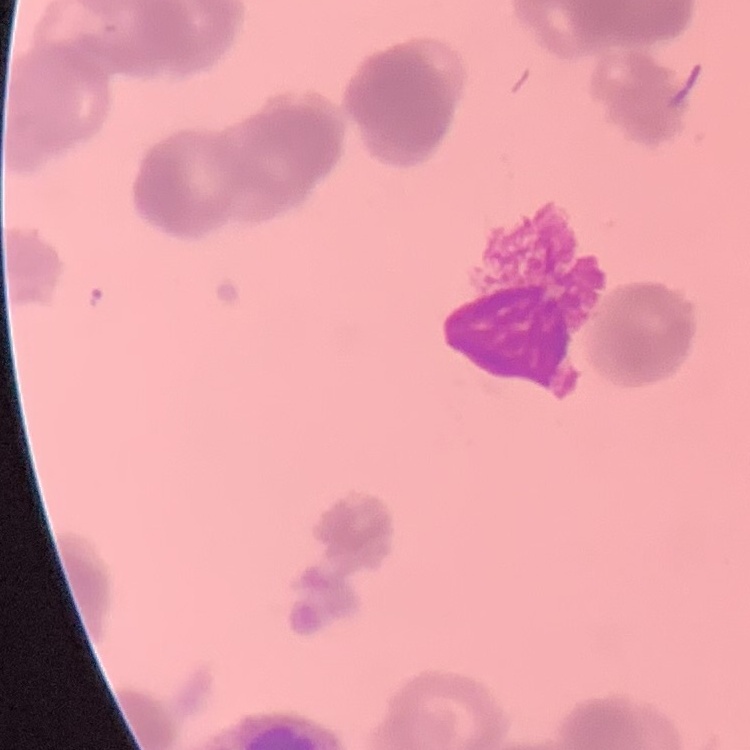

Summary:
  - Erythrocyte morphology: rouleaux formation
  - Preparation: thin blood film
  - Image type: one tile cut from a larger photomicrograph
  - Stain: Field's or Giemsa